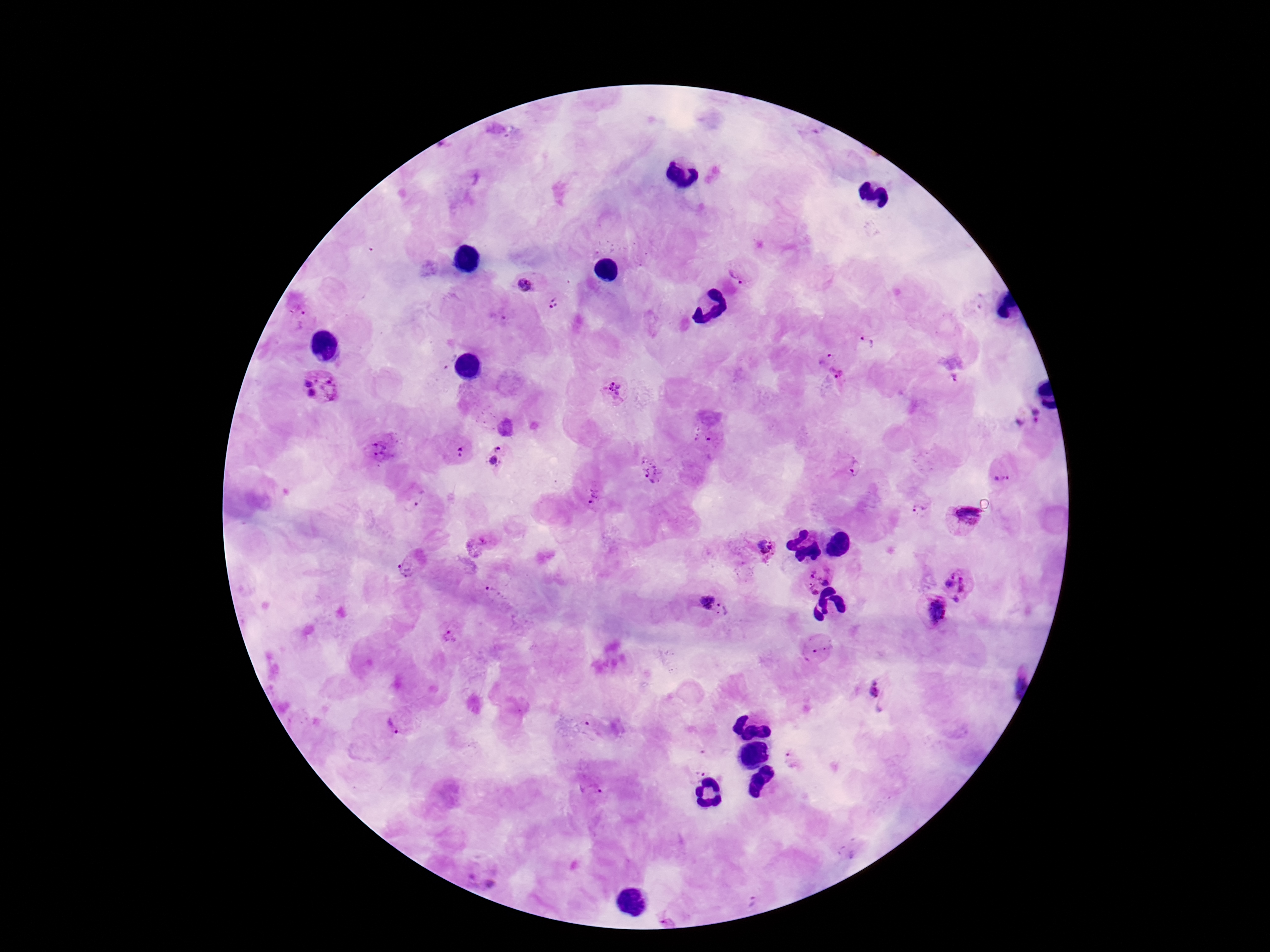 Approximate centers as {x, y} in pixels. Plasmodium parasite locations: {738, 273}, {527, 281}, {555, 303}, {297, 306}, {501, 317}, {868, 342}, {826, 357}, {838, 375}, {955, 380}, {321, 387}, {614, 390}, {1028, 417}, {505, 427}, {702, 435}, {379, 450}, {460, 452}, {497, 458}, {855, 468}, {651, 469}, {1002, 473}, {594, 496}, {413, 502}, {920, 505}, {963, 516}, {767, 550}, {411, 565}, {817, 576}, {959, 583}, {493, 593}, {714, 605}, {931, 609}, {452, 635}, {817, 649}, {876, 690}, {397, 724}, {794, 760}, {697, 769}, {593, 789}, {483, 876}, {753, 899}. Image is 1270×952 pixels. One field from this slide. Photographed through the microscope eyepiece with a smartphone camera. Patient malaria status: infected. Giemsa stain. 100x magnification. Thick blood film.